Outline each Plasmodium falciparum-infected red blood cell.
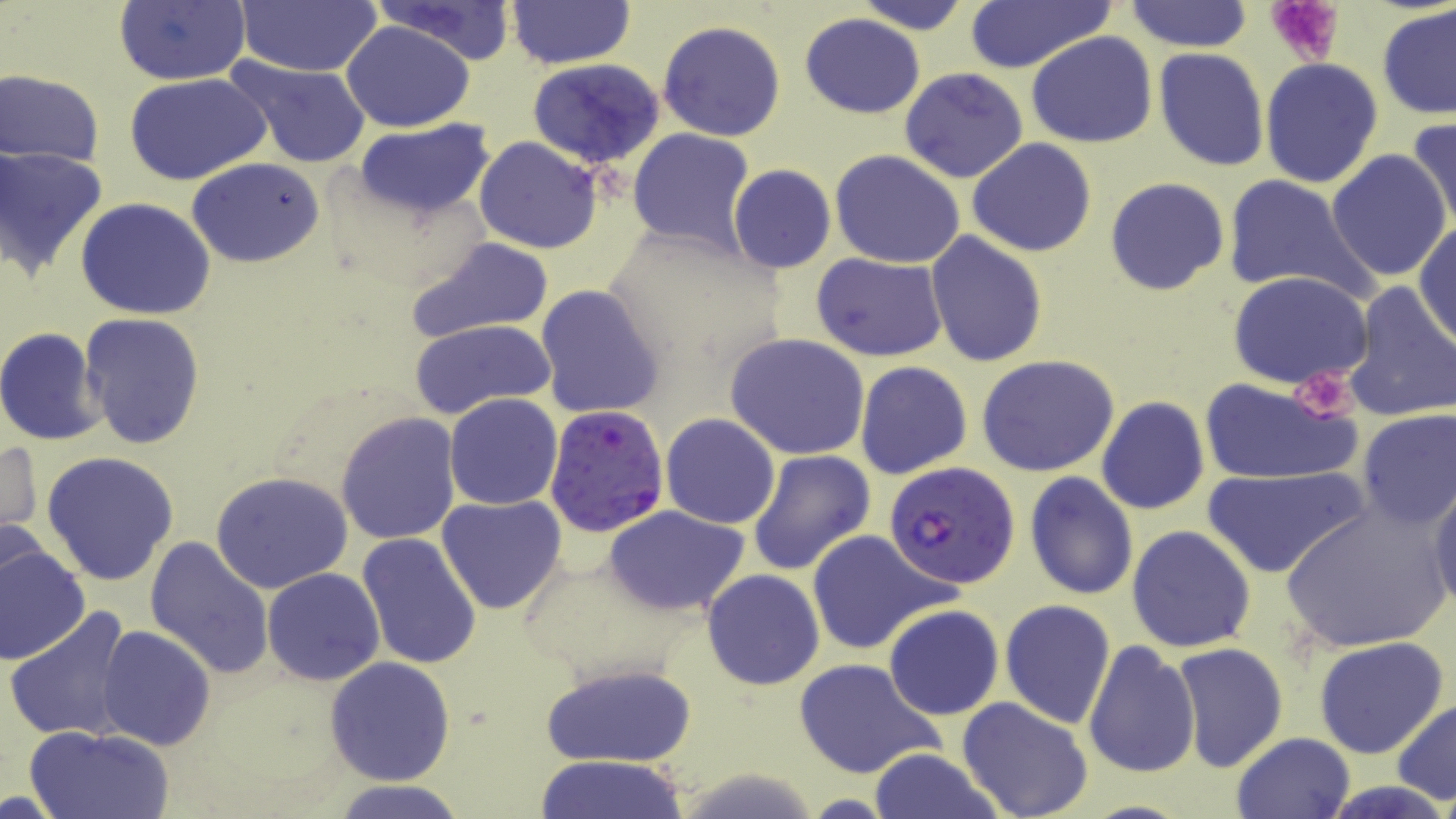
Approximate bounding boxes as (x1, y1, x2, y2) in pixels.
Plasmodium falciparum-infected red blood cells: (544, 405, 670, 538), (885, 461, 1021, 591).

Summary:
  - Platelet locations: (1266, 0, 1346, 66), (1289, 367, 1362, 423)
  - Uninfected red blood cell locations: (113, 0, 249, 86), (371, 0, 519, 64), (853, 0, 972, 34), (236, 1, 385, 75), (1123, 1, 1254, 53), (962, 2, 1116, 75), (1376, 2, 1456, 120), (505, 3, 635, 70), (510, 4, 642, 141), (800, 13, 926, 118), (340, 20, 476, 132), (658, 20, 786, 141), (1027, 32, 1159, 148), (1153, 47, 1270, 172), (224, 54, 373, 168), (1260, 58, 1384, 188), (528, 59, 664, 168), (900, 67, 1030, 184), (2, 69, 105, 167), (127, 74, 271, 185), (1405, 118, 1456, 238), (354, 119, 494, 219), (628, 129, 756, 255), (474, 136, 602, 255), (967, 137, 1096, 256), (1, 146, 108, 281), (1327, 148, 1454, 284), (830, 150, 965, 270), (186, 157, 325, 268), (727, 165, 837, 273), (1222, 174, 1376, 303), (1105, 177, 1230, 296), (75, 198, 219, 320), (1413, 222, 1456, 347), (924, 231, 1047, 368), (405, 236, 557, 345), (812, 253, 949, 362), (1228, 271, 1374, 390), (1340, 280, 1456, 423), (535, 285, 664, 419), (79, 313, 204, 451), (409, 317, 560, 420), (0, 326, 108, 448), (726, 333, 873, 461), (977, 354, 1121, 477), (855, 361, 972, 480), (1198, 378, 1363, 485), (445, 393, 563, 510), (1096, 397, 1209, 515), (1356, 408, 1455, 529), (335, 411, 461, 545), (660, 413, 780, 529), (1, 437, 42, 551), (748, 449, 877, 576), (41, 452, 178, 586), (1204, 465, 1365, 580), (210, 471, 353, 593), (1025, 472, 1139, 599), (1428, 482, 1456, 614), (436, 494, 567, 616), (1279, 499, 1449, 652), (604, 505, 749, 614), (1126, 525, 1256, 652), (804, 530, 950, 654), (356, 532, 483, 670), (144, 535, 275, 679), (0, 538, 91, 667), (262, 567, 385, 686), (700, 568, 825, 690), (1000, 599, 1116, 728), (882, 604, 1004, 720), (6, 606, 135, 744), (98, 626, 216, 750), (1312, 637, 1450, 759), (1083, 640, 1200, 778), (1170, 642, 1288, 772), (324, 657, 456, 786), (793, 657, 946, 780), (541, 660, 698, 768), (956, 697, 1094, 819), (1392, 698, 1456, 804), (25, 723, 175, 819), (1231, 731, 1354, 818), (866, 749, 1003, 819), (533, 755, 692, 819), (327, 780, 474, 818)
  - Slide-level diagnosis: Plasmodium falciparum
  - Preparation: thin blood smear
  - Stain: May-Grünwald-Giemsa
  - Field of view: single
  - Magnification: 1000x
  - Image size: 1456×819 pixels
  - Modality: light microscopy